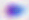

Toxoplasma gondii is seen. Micrograph. Captured at 400x magnification.